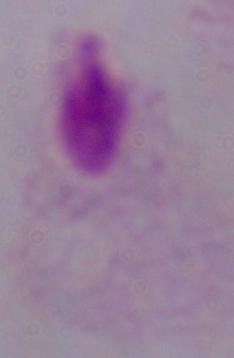
{
  "modality": "photomicrograph",
  "identification": "trichomonad",
  "magnification": "1000x"
}